Point out each malaria parasite and each leukocyte.
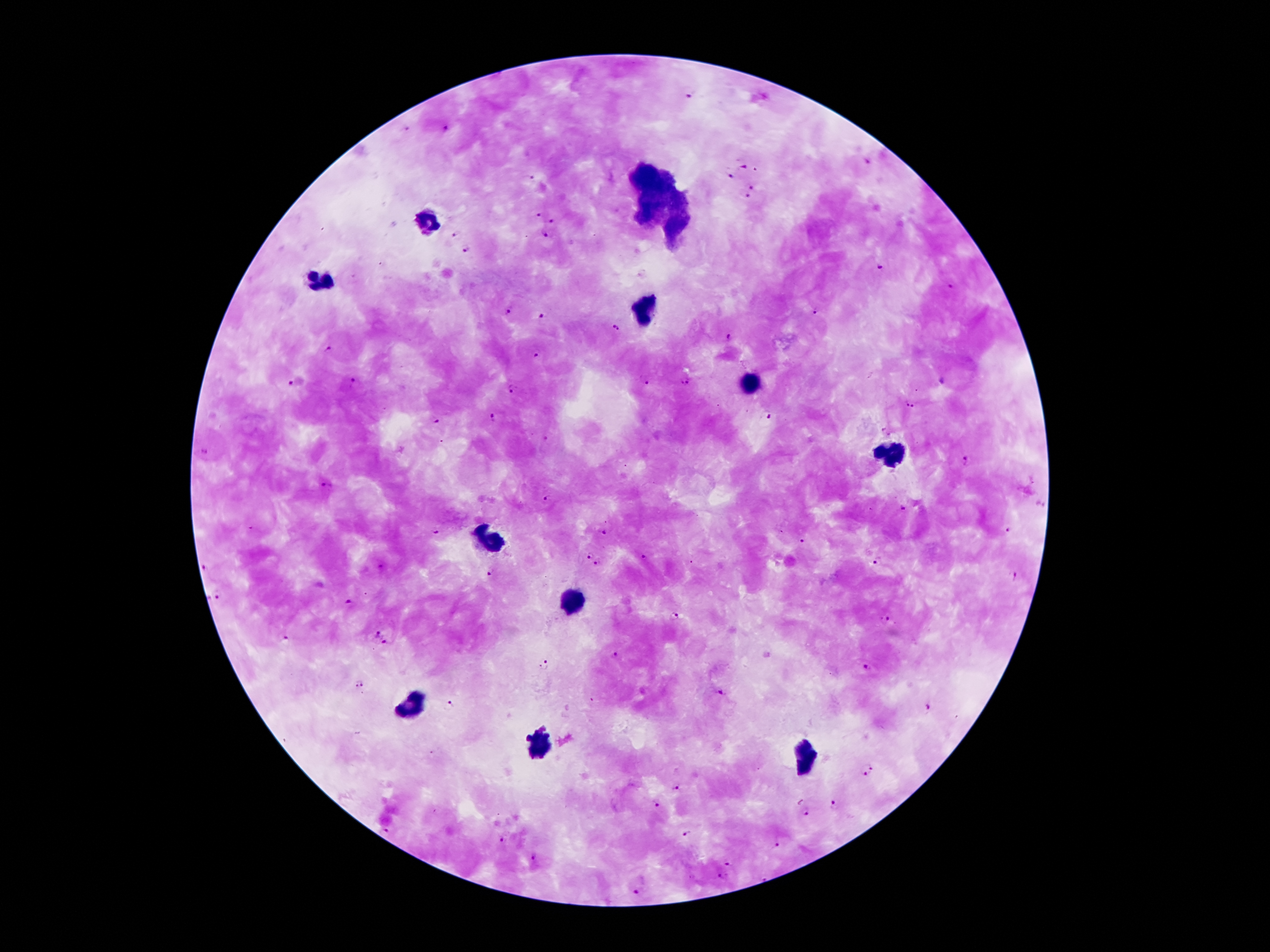
Approximate centers as [x, y] in pixels.
Malaria parasites: [690, 97], [405, 130], [446, 130], [867, 160], [743, 167], [530, 178], [730, 178], [751, 186], [747, 197], [538, 216], [553, 221], [457, 235], [546, 238], [466, 252], [882, 266], [950, 288], [817, 311], [508, 312], [541, 315], [614, 328], [727, 338], [327, 351], [535, 355], [646, 379], [352, 382], [686, 382], [290, 383], [944, 383], [511, 389], [909, 405], [492, 418], [772, 418], [436, 421], [886, 430], [205, 453], [964, 459], [326, 484], [547, 498], [1040, 503], [902, 507], [1008, 530], [436, 531], [604, 533], [801, 541], [588, 556], [644, 558], [877, 561], [598, 564], [205, 568], [491, 571], [1011, 575], [218, 596], [348, 603], [674, 616], [887, 620], [378, 632], [283, 638], [384, 643], [616, 655], [544, 665], [866, 668], [361, 682], [719, 690], [451, 703], [926, 709], [866, 769], [675, 787], [834, 804], [653, 805], [805, 814], [384, 832], [685, 834], [502, 839], [776, 844], [533, 859], [729, 863], [720, 878], [635, 892].
Leukocytes: [648, 174], [666, 182], [655, 198], [678, 201], [646, 215], [428, 222], [676, 228], [317, 279], [642, 311], [750, 383], [891, 453], [490, 538], [571, 601], [410, 705], [539, 742], [807, 760].

image size = 1270×952 pixels
patient malaria status = positive for Plasmodium falciparum
capture = smartphone camera through the microscope eyepiece
magnification = 100x
stain = Giemsa
field of view = single
preparation = thick peripheral-blood smear